Describe the morphology of the red blood cells.
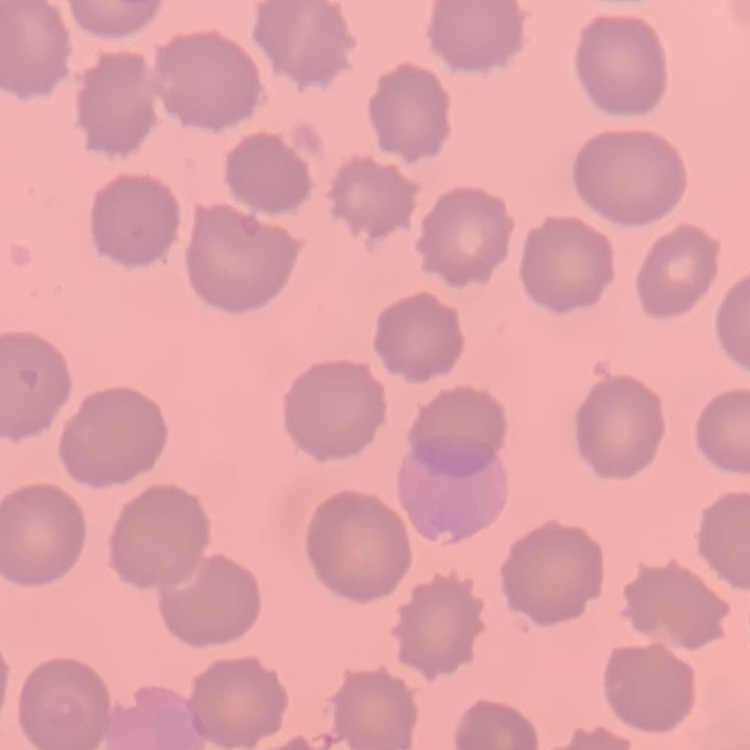

They show no rouleaux formation.

image type = square crop of a larger photomicrograph
stain = Field's or Giemsa
preparation = thin blood film